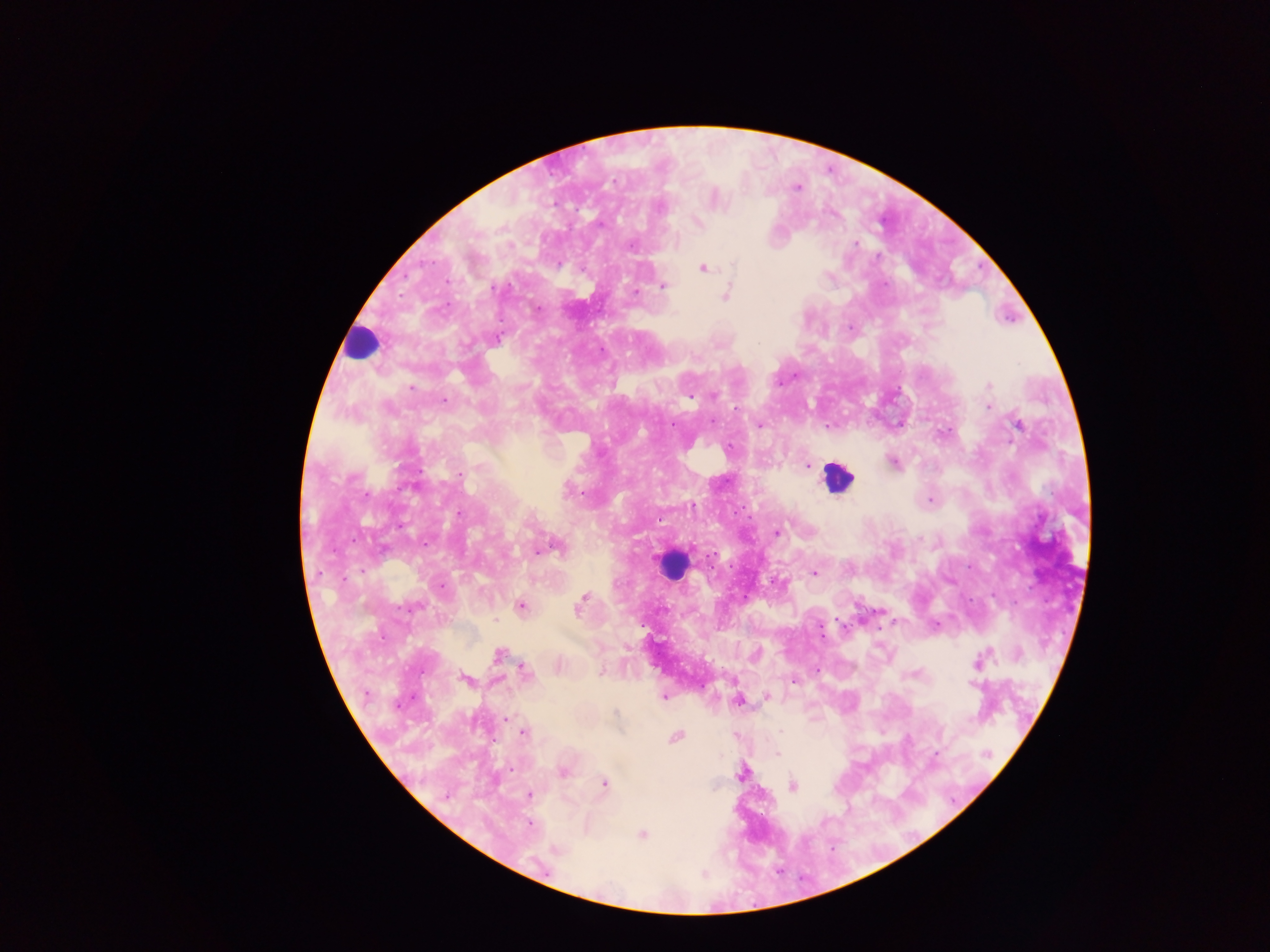 Approximate centers as (x, y) in pixels. Malaria parasite locations: (795, 187), (714, 198), (698, 222), (702, 267), (663, 286), (635, 291), (726, 293), (851, 328), (988, 385), (411, 388), (713, 395), (445, 401), (988, 407), (899, 423), (1017, 423), (759, 424), (830, 426), (893, 462), (807, 465), (459, 474), (930, 501), (777, 533), (552, 547), (814, 572), (777, 581), (581, 601), (520, 605), (936, 624), (499, 654), (755, 655), (978, 661), (558, 666), (816, 670), (523, 672), (600, 673), (465, 679), (794, 680), (664, 695), (767, 696), (738, 699), (506, 717), (524, 732), (675, 737), (776, 753), (562, 771), (742, 772), (604, 783), (791, 786), (528, 794), (528, 824), (641, 835). Leukocyte locations: (360, 345), (837, 478), (673, 564). Thick blood film. Collected in Ghana. One field of view. Image is 1270×952 pixels. Photographed through a microscope with a mobile-phone camera.